Assess this cell for malaria.
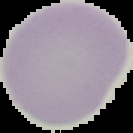
It is uninfected.

{
  "image_size": "133×133 pixels",
  "preparation": "thin blood smear",
  "image_type": "segmented cell region on a black background"
}